Classify this cell by malaria status.
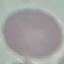
Uninfected.

preparation: thin smear
image_type: automatically extracted cell patch, resized to 64 × 64 pixels
stain: Giemsa
capture: smartphone through the microscope eyepiece